Classify this cell by malaria status.
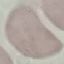

It is uninfected.

Summary:
  - Capture: smartphone through the microscope eyepiece
  - Image type: cell patch, automatically extracted from a larger field of view and resized to 64 × 64 pixels
  - Preparation: thin blood smear
  - Stain: Giemsa